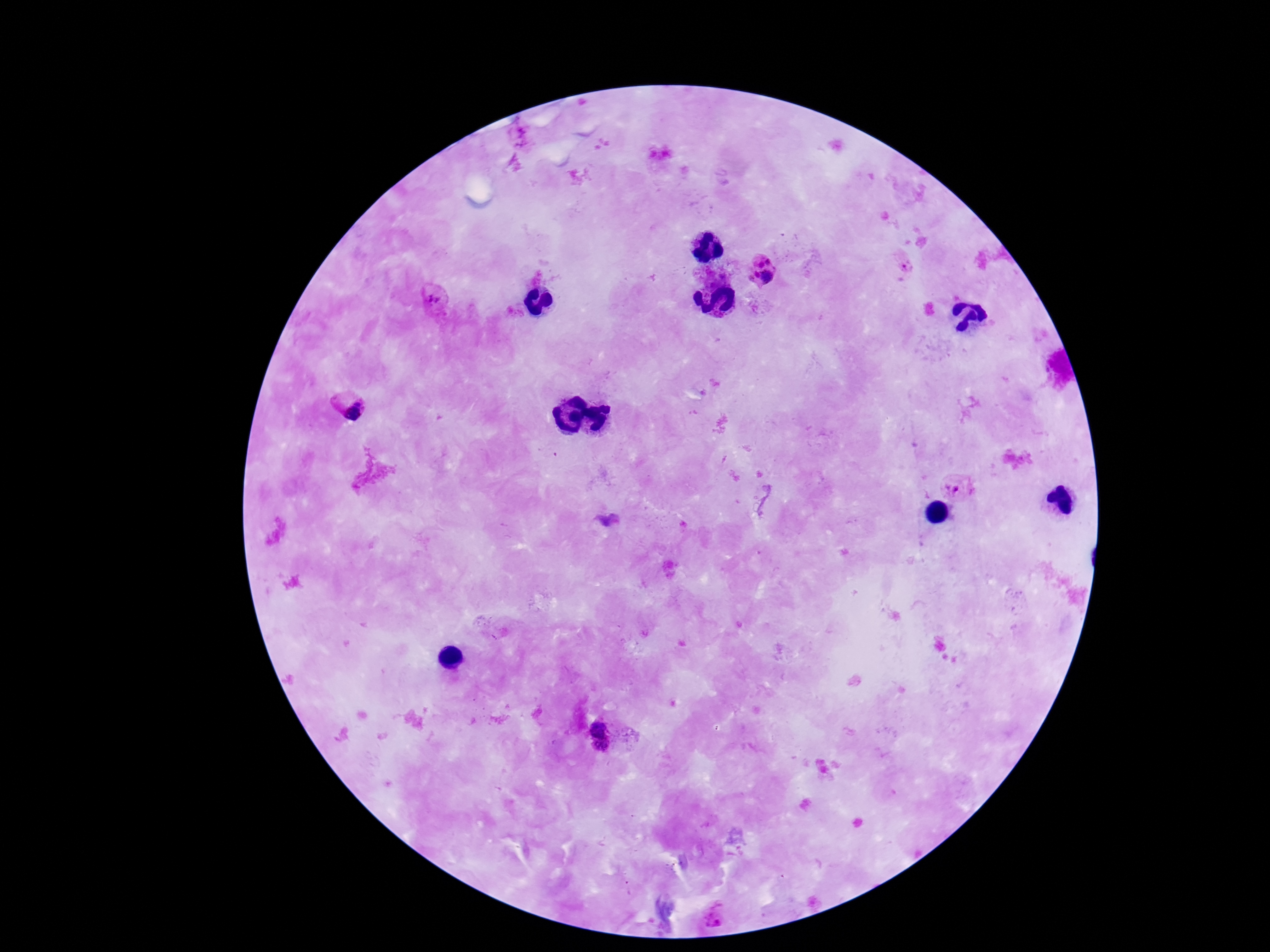 Approximate centers as (x, y) in pixels. Plasmodium parasite locations: (522, 137), (769, 261), (760, 264), (903, 264), (756, 273), (767, 276), (751, 279), (434, 297), (359, 400), (352, 415), (958, 484), (598, 729), (601, 749), (714, 917). 100x magnification. Thick blood film. Giemsa stain. Patient malaria status: infected. Smartphone photograph taken through the microscope eyepiece. Image is 1270×952 pixels. One field from this slide.